Locate every blood parasite and identify its species.
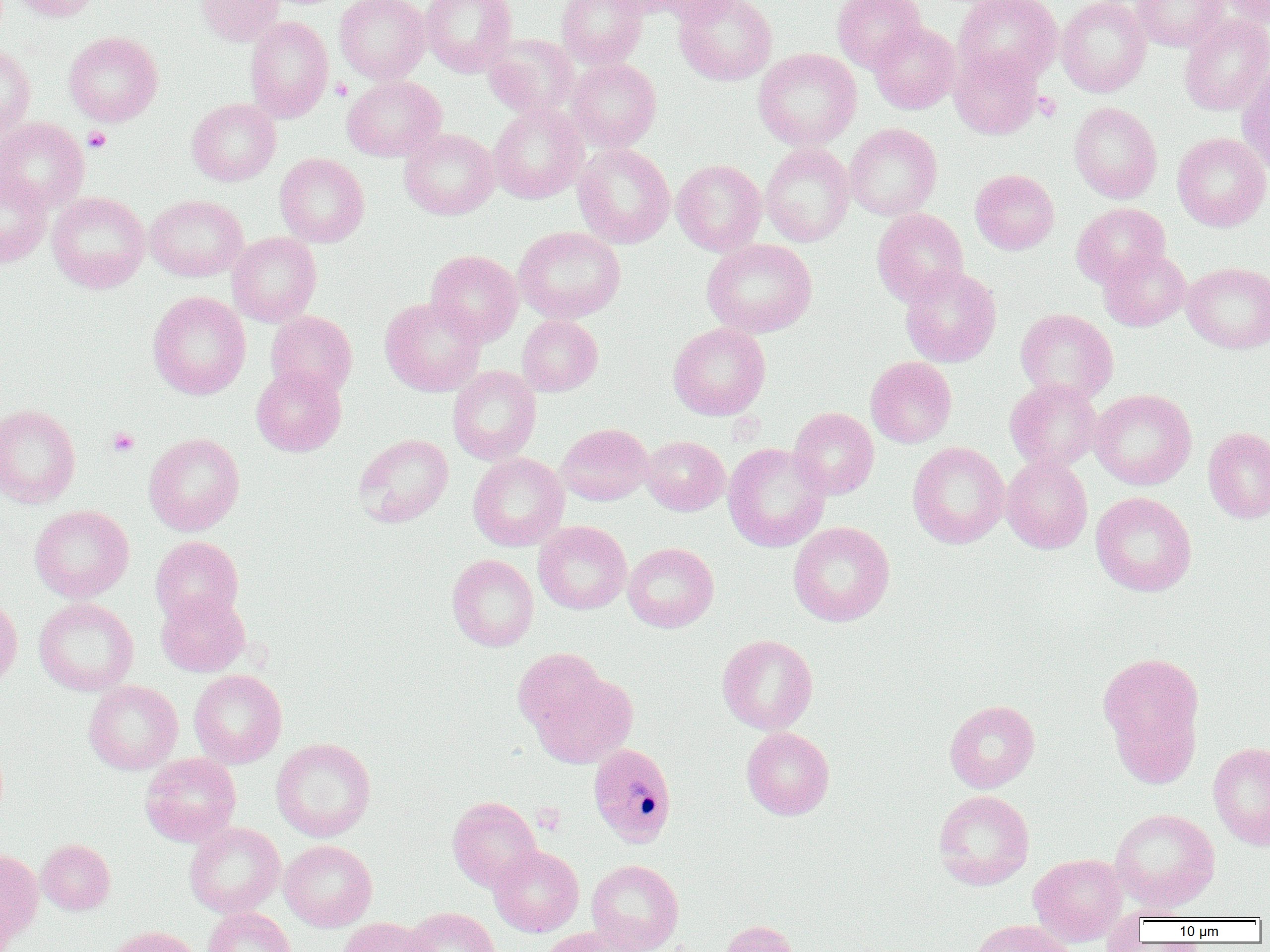

Approximate bounding boxes as named x1/y1/x2/y2 corners in pixels.
Plasmodium malariae-infected red blood cells: (x1=587, y1=741, x2=677, y2=847).
No Plasmodium falciparum, Plasmodium ovale, Plasmodium vivax, Babesia divergens, or Trypanosoma brucei observed.

slide-level diagnosis = Plasmodium malariae
field of view = single
platelet locations = approximate bounding boxes as named x1/y1/x2/y2 corners in pixels: (x1=330, y1=78, x2=352, y2=101), (x1=1033, y1=92, x2=1061, y2=120), (x1=83, y1=127, x2=111, y2=152), (x1=107, y1=428, x2=140, y2=456), (x1=532, y1=802, x2=565, y2=833)
modality = optical microscopy
image size = 1270×952 pixels
uninfected red blood cell locations = approximate bounding boxes as named x1/y1/x2/y2 corners in pixels: (x1=8, y1=0, x2=99, y2=21), (x1=197, y1=0, x2=283, y2=45), (x1=335, y1=0, x2=430, y2=84), (x1=420, y1=0, x2=517, y2=77), (x1=557, y1=0, x2=648, y2=69), (x1=645, y1=0, x2=747, y2=24), (x1=675, y1=0, x2=777, y2=85), (x1=832, y1=0, x2=925, y2=73), (x1=955, y1=0, x2=1062, y2=84), (x1=1056, y1=0, x2=1150, y2=97), (x1=1132, y1=0, x2=1227, y2=51), (x1=1219, y1=0, x2=1270, y2=26), (x1=1062, y1=2, x2=1153, y2=202), (x1=1179, y1=15, x2=1270, y2=115), (x1=245, y1=17, x2=333, y2=122), (x1=868, y1=21, x2=960, y2=114), (x1=64, y1=31, x2=163, y2=126), (x1=485, y1=33, x2=579, y2=119), (x1=0, y1=44, x2=36, y2=139), (x1=950, y1=47, x2=1042, y2=139), (x1=754, y1=48, x2=861, y2=150), (x1=566, y1=58, x2=661, y2=151), (x1=1236, y1=64, x2=1270, y2=175), (x1=342, y1=75, x2=446, y2=161), (x1=187, y1=98, x2=281, y2=186), (x1=488, y1=102, x2=587, y2=203), (x1=1069, y1=102, x2=1162, y2=203), (x1=0, y1=117, x2=89, y2=212), (x1=845, y1=123, x2=942, y2=221), (x1=400, y1=128, x2=499, y2=220), (x1=1172, y1=132, x2=1270, y2=231), (x1=573, y1=143, x2=675, y2=248), (x1=760, y1=143, x2=855, y2=246), (x1=275, y1=153, x2=370, y2=247), (x1=671, y1=159, x2=766, y2=255), (x1=970, y1=169, x2=1059, y2=254), (x1=0, y1=170, x2=51, y2=268), (x1=47, y1=191, x2=150, y2=293), (x1=145, y1=194, x2=248, y2=281), (x1=1071, y1=202, x2=1171, y2=288), (x1=872, y1=208, x2=968, y2=306), (x1=514, y1=226, x2=626, y2=323), (x1=227, y1=232, x2=321, y2=327), (x1=702, y1=238, x2=817, y2=338), (x1=1099, y1=248, x2=1190, y2=331), (x1=425, y1=250, x2=523, y2=346), (x1=1182, y1=262, x2=1270, y2=353), (x1=899, y1=265, x2=1001, y2=367), (x1=148, y1=291, x2=250, y2=399), (x1=380, y1=297, x2=486, y2=396), (x1=1015, y1=308, x2=1118, y2=404), (x1=265, y1=311, x2=357, y2=399), (x1=517, y1=315, x2=602, y2=396), (x1=668, y1=323, x2=771, y2=420), (x1=865, y1=357, x2=957, y2=447), (x1=251, y1=366, x2=346, y2=456), (x1=447, y1=366, x2=541, y2=465), (x1=1005, y1=378, x2=1103, y2=472), (x1=1090, y1=388, x2=1196, y2=490), (x1=0, y1=404, x2=81, y2=508), (x1=788, y1=407, x2=879, y2=499), (x1=556, y1=423, x2=653, y2=506), (x1=1203, y1=427, x2=1270, y2=523), (x1=144, y1=432, x2=245, y2=536), (x1=354, y1=433, x2=453, y2=527), (x1=641, y1=435, x2=729, y2=515), (x1=908, y1=442, x2=1010, y2=549), (x1=723, y1=443, x2=830, y2=551), (x1=468, y1=452, x2=568, y2=551), (x1=1001, y1=455, x2=1093, y2=553), (x1=1090, y1=491, x2=1197, y2=597), (x1=29, y1=505, x2=134, y2=602), (x1=534, y1=521, x2=632, y2=614), (x1=788, y1=521, x2=894, y2=626), (x1=151, y1=535, x2=243, y2=626), (x1=622, y1=542, x2=719, y2=632), (x1=447, y1=554, x2=539, y2=651), (x1=156, y1=591, x2=250, y2=677), (x1=0, y1=596, x2=22, y2=694), (x1=34, y1=598, x2=139, y2=696), (x1=717, y1=634, x2=818, y2=735), (x1=513, y1=648, x2=607, y2=739), (x1=1097, y1=650, x2=1206, y2=767), (x1=188, y1=669, x2=287, y2=768), (x1=530, y1=670, x2=637, y2=769), (x1=84, y1=680, x2=183, y2=774), (x1=944, y1=700, x2=1040, y2=793), (x1=1108, y1=700, x2=1201, y2=788), (x1=741, y1=727, x2=835, y2=820), (x1=271, y1=737, x2=376, y2=842), (x1=1208, y1=741, x2=1270, y2=850), (x1=140, y1=753, x2=241, y2=846), (x1=933, y1=789, x2=1035, y2=890), (x1=447, y1=797, x2=542, y2=891), (x1=1109, y1=808, x2=1220, y2=912), (x1=184, y1=822, x2=285, y2=917), (x1=37, y1=839, x2=115, y2=914), (x1=279, y1=839, x2=377, y2=931), (x1=489, y1=845, x2=583, y2=936), (x1=0, y1=848, x2=42, y2=943), (x1=1029, y1=853, x2=1127, y2=946), (x1=586, y1=859, x2=684, y2=952), (x1=0, y1=889, x2=16, y2=952), (x1=203, y1=907, x2=296, y2=952), (x1=403, y1=907, x2=500, y2=952), (x1=339, y1=917, x2=435, y2=952), (x1=968, y1=919, x2=1078, y2=952), (x1=719, y1=920, x2=804, y2=952), (x1=103, y1=926, x2=203, y2=952), (x1=537, y1=927, x2=640, y2=952)
preparation = thin blood smear
magnification = 1000x